Describe the morphology of the erythrocytes.
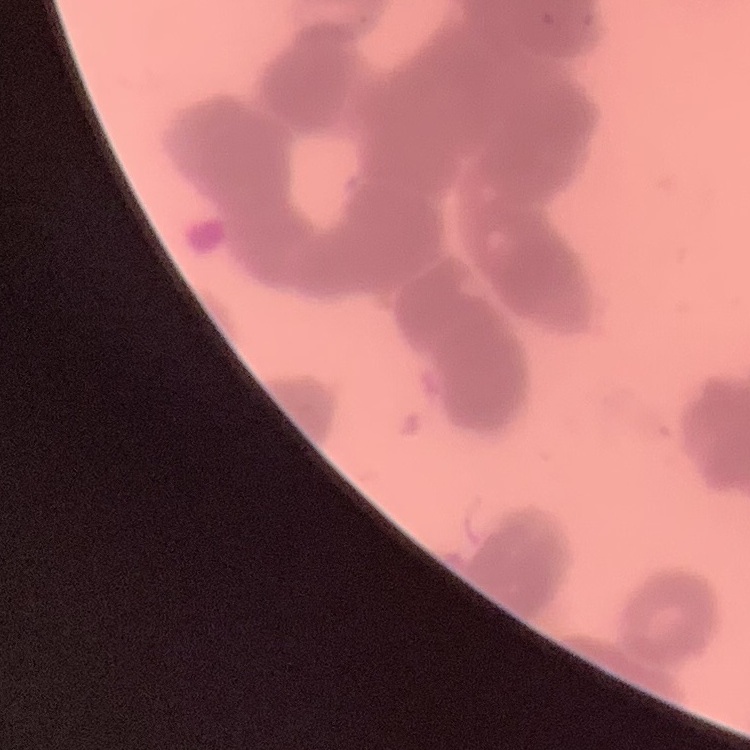
Rouleaux formation.

Summary:
  - Stain: Field's or Giemsa
  - Image type: square crop of a larger photomicrograph
  - Preparation: thin peripheral smear